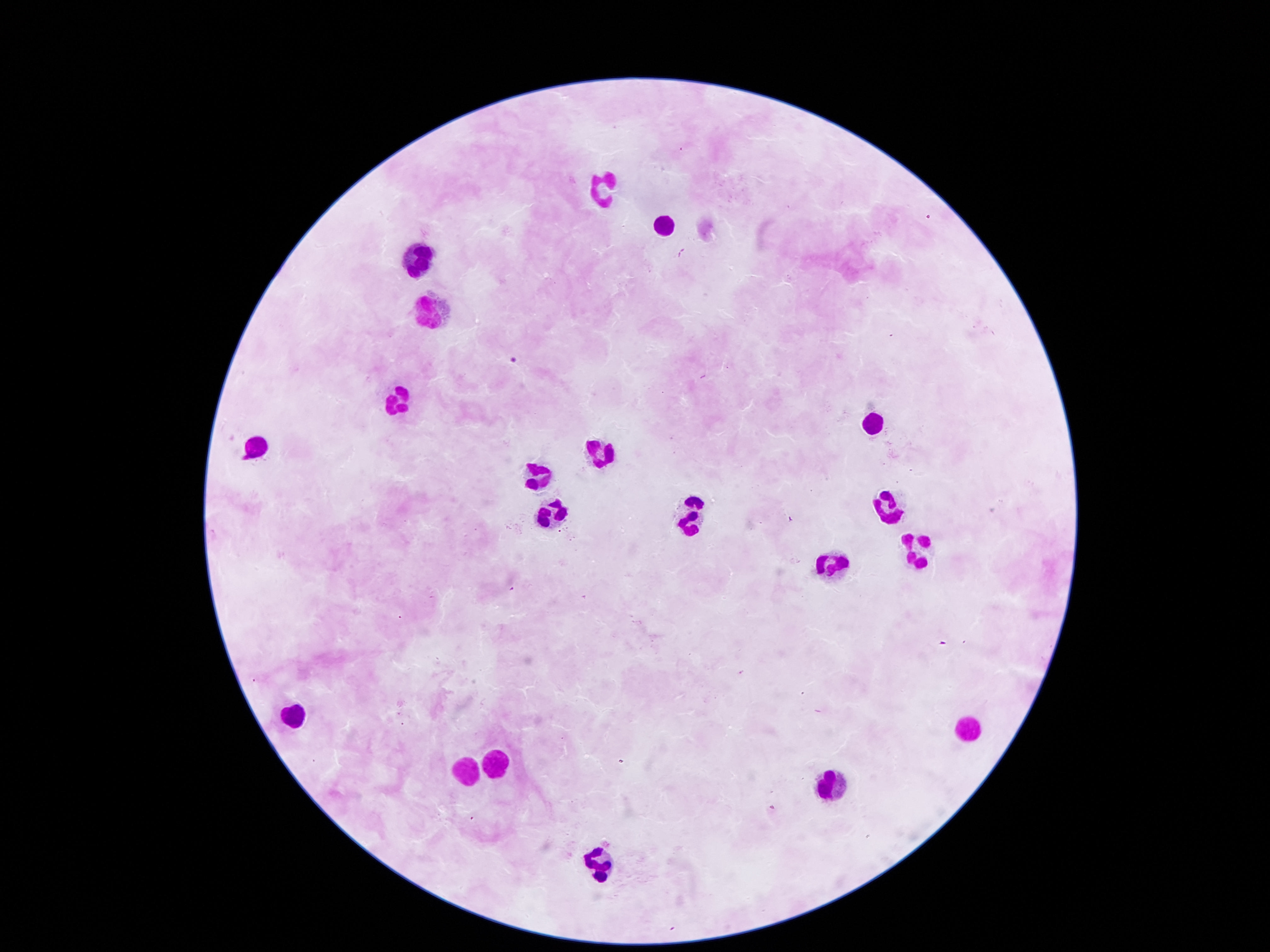
Approximate centers as [x, y] in pixels. Leukocyte locations: [603, 187], [663, 227], [412, 259], [434, 308], [403, 397], [873, 420], [255, 446], [596, 449], [539, 476], [888, 502], [544, 515], [691, 517], [919, 545], [835, 564], [289, 713], [969, 727], [496, 759], [463, 767], [831, 778], [605, 858]. Image is 1270×952 pixels. 100x magnification. Giemsa-stained preparation. Thick blood film. Patient malaria status: uninfected. Smartphone photograph taken through the microscope eyepiece. Single field of view.